State which cell type is depicted.
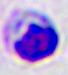

A leukocyte.

magnification: 400x
modality: photomicrograph